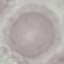

Summary:
  - Result: no malaria parasites detected
  - Image type: cell patch, automatically extracted from a larger field of view and resized to 64 × 64 pixels
  - Capture: smartphone camera at the microscope eyepiece
  - Preparation: thin blood smear
  - Stain: Giemsa